Classify this cell by malaria status.
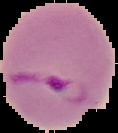

It is parasitized.

From a thin blood smear. Cell region segmented out of the field of view; the surrounding area is masked to black. Image is 118×133 pixels.